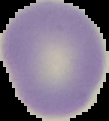
Result: negative for malaria parasites. The area outside the segmented cell region is set to black. From a thin blood smear. Image is 109×121 pixels.